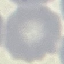
Summary:
  - Malaria status: uninfected
  - Preparation: thin blood film
  - Stain: Giemsa
  - Image type: cell patch, automatically extracted from a larger field of view and resized to 64 × 64 pixels
  - Capture: smartphone camera at the microscope eyepiece